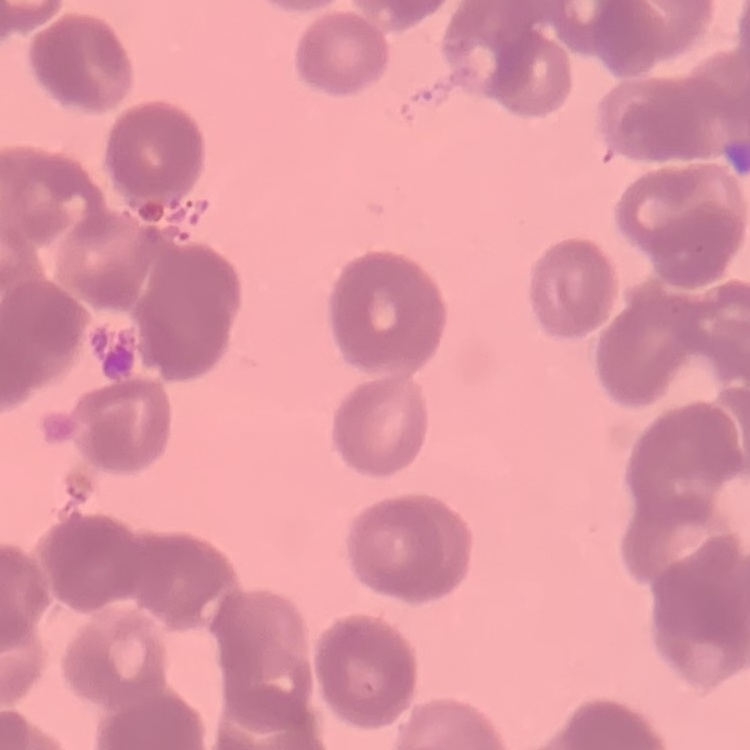 The erythrocytes exhibit rouleaux formation. Square crop of a larger photomicrograph. Thin peripheral smear. Field's or Giemsa stain.